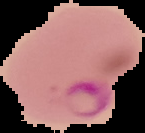
{
  "preparation": "thin blood film",
  "malaria_status": "parasitized",
  "image_type": "segmented cell region on a black background",
  "image_size": "145×133 pixels"
}